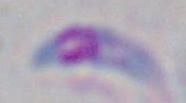

magnification = 1000x
identification = Toxoplasma gondii
modality = photomicrograph